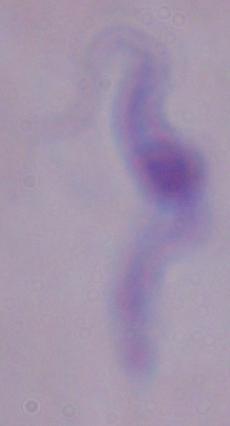
Summary:
  - Magnification: 1000x
  - Identification: trypanosome
  - Modality: photomicrograph